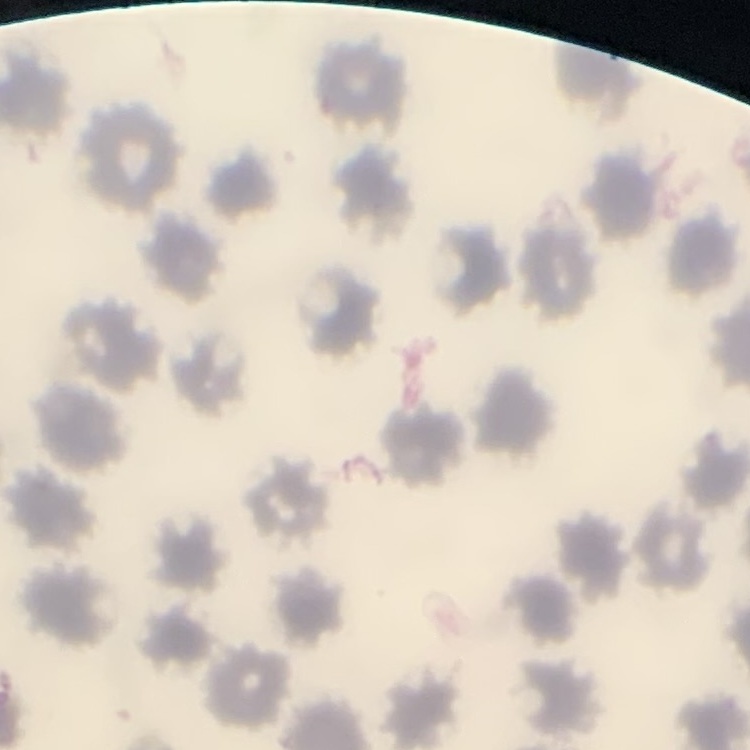

erythrocyte morphology = no rouleaux formation
stain = Field's or Giemsa
preparation = thin blood smear
image type = square crop of a larger photomicrograph